Outline each blood parasite and name the species.
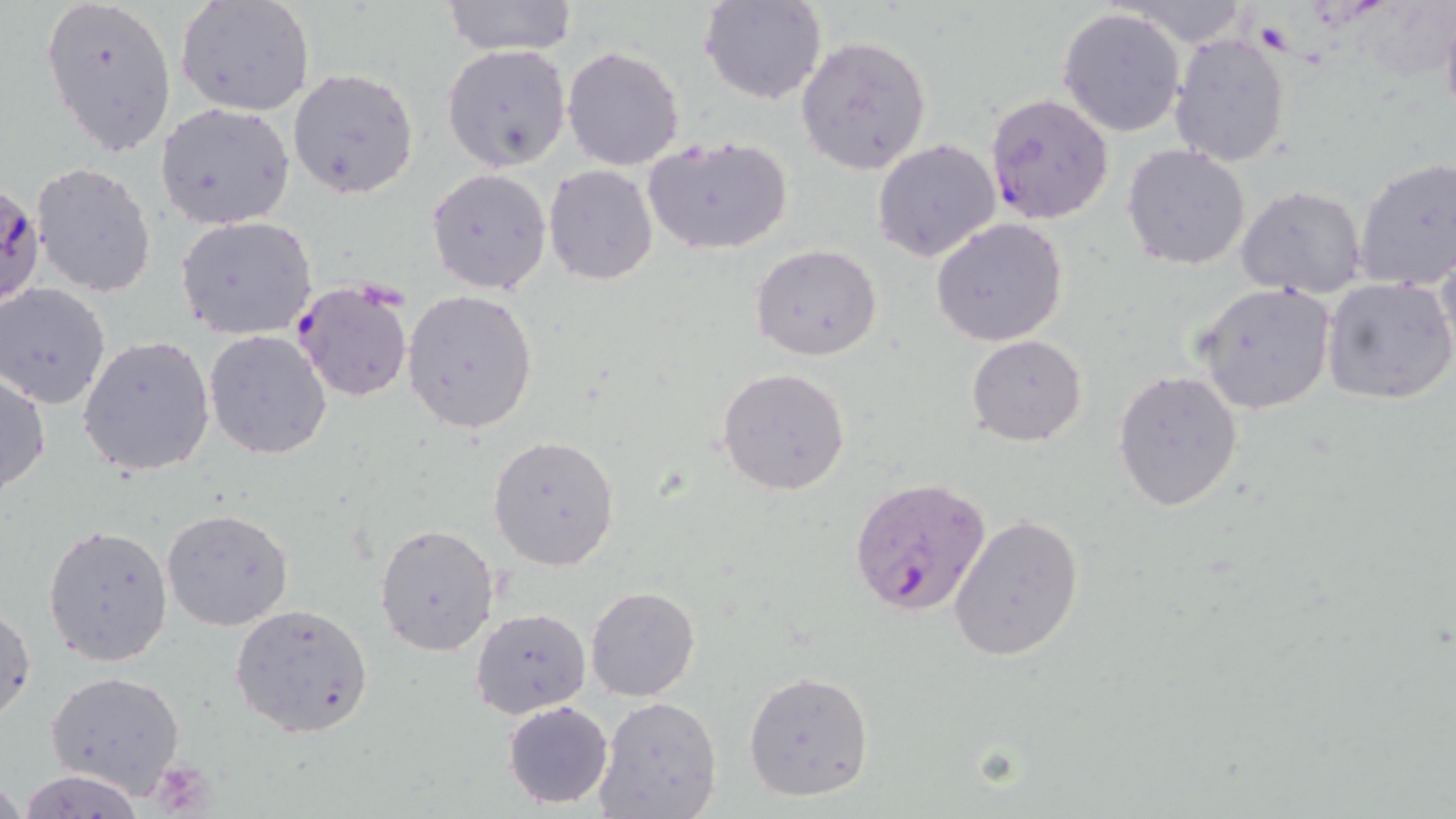

Approximate bounding boxes as (x1, y1, x2, y2) in pixels.
Plasmodium falciparum-infected red blood cells: (983, 92, 1115, 224), (0, 183, 44, 310), (293, 281, 413, 402), (847, 475, 990, 616).
No Plasmodium ovale, Plasmodium malariae, Plasmodium vivax, Babesia divergens, or Trypanosoma brucei observed.

Summary:
  - Platelet locations: (1254, 19, 1296, 52), (151, 759, 216, 815)
  - Uninfected red blood cell locations: (42, 0, 178, 159), (175, 0, 316, 117), (699, 0, 825, 105), (441, 1, 578, 56), (1114, 1, 1254, 44), (1440, 2, 1456, 127), (1057, 7, 1186, 136), (1168, 33, 1291, 169), (794, 35, 932, 175), (439, 44, 571, 172), (563, 46, 684, 171), (287, 67, 418, 198), (156, 103, 295, 230), (642, 135, 795, 257), (873, 139, 1000, 261), (1121, 144, 1251, 270), (1352, 158, 1456, 291), (31, 162, 157, 297), (543, 166, 658, 284), (427, 168, 552, 294), (1235, 184, 1367, 298), (175, 215, 317, 340), (930, 218, 1069, 346), (750, 243, 883, 362), (1435, 244, 1456, 365), (1323, 276, 1456, 407), (1193, 282, 1336, 415), (1, 283, 114, 410), (402, 289, 538, 434), (204, 331, 331, 460), (965, 335, 1089, 446), (80, 336, 215, 476), (717, 367, 853, 498), (1111, 369, 1243, 511), (1, 371, 51, 498), (488, 436, 619, 572), (162, 507, 294, 630), (948, 514, 1083, 661), (43, 524, 173, 668), (375, 524, 499, 656), (585, 586, 700, 701), (0, 603, 35, 725), (231, 603, 374, 739), (470, 608, 591, 718), (47, 671, 186, 795), (743, 671, 874, 802), (594, 695, 722, 819), (503, 700, 614, 808), (17, 769, 145, 818), (0, 776, 24, 817)
  - Slide-level diagnosis: Plasmodium falciparum
  - Stain: May-Grünwald-Giemsa
  - Image size: 1456×819 pixels
  - Magnification: 1000x
  - Modality: optical microscopy
  - Field of view: one of a larger specimen
  - Preparation: thin blood smear